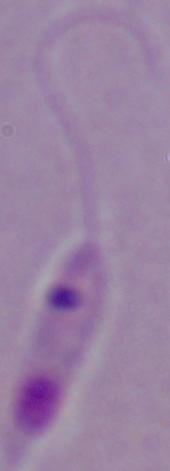
Summary:
  - Magnification: 1000x
  - Identification: Leishmania
  - Modality: photomicrograph